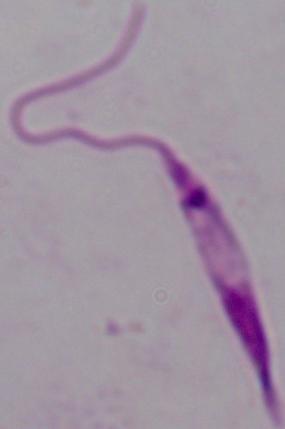

identification = Leishmania
magnification = 1000x
modality = photomicrograph